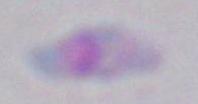
Summary:
  - Modality: micrograph
  - Magnification: 1000x
  - Identification: Toxoplasma gondii